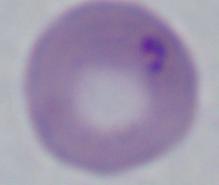

Summary:
  - Modality: micrograph
  - Magnification: 1000x
  - Identification: Babesia